Assess this cell for malaria.
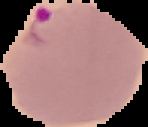
Parasitized.

image size = 148×127 pixels
image type = segmented cell region on a black background
preparation = thin blood smear